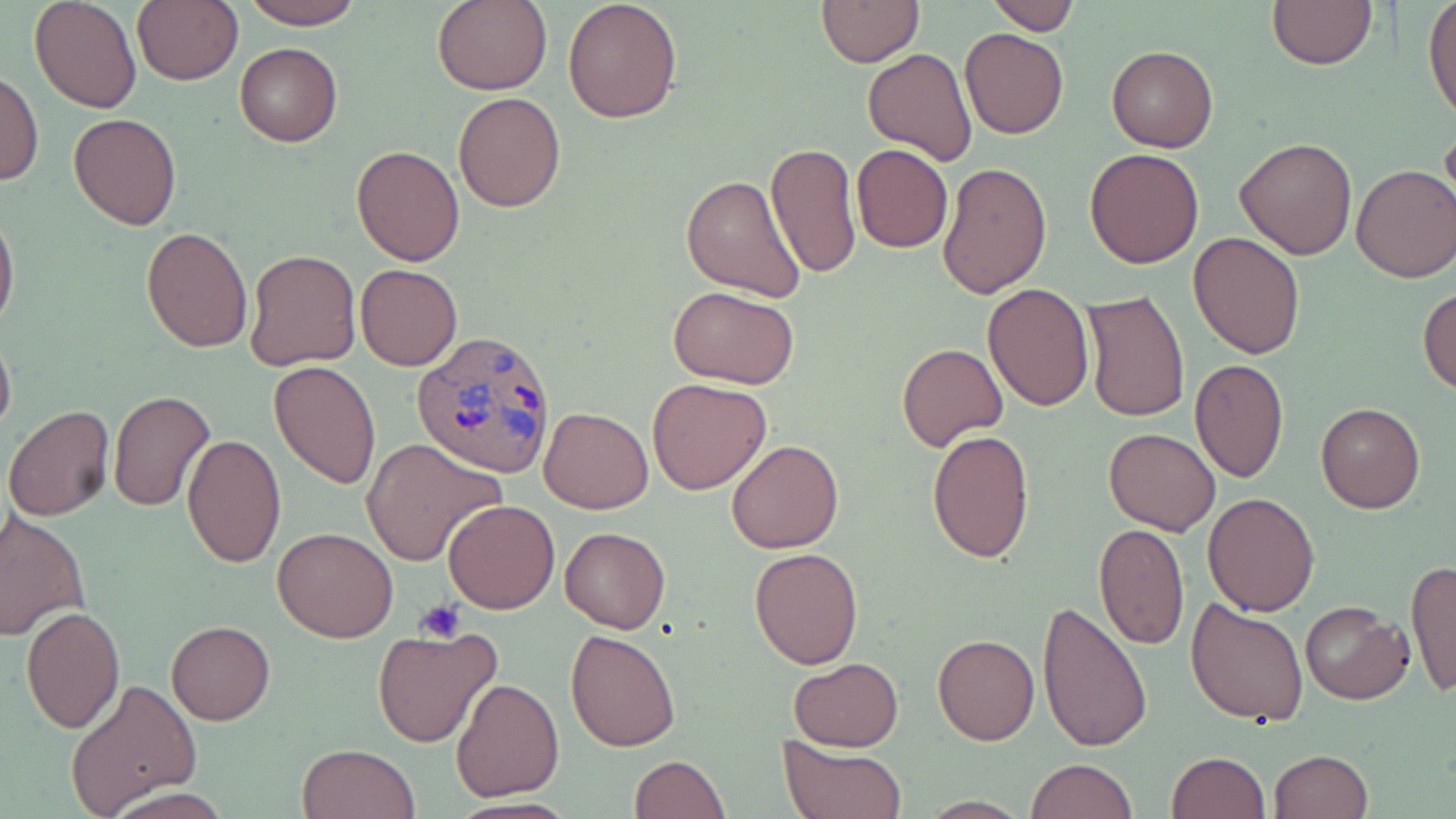 Approximate bounding boxes as [x1, y1, x2, y2] in pixels. Plasmodium ovale-infected red blood cell locations: [411, 327, 557, 476]. Uninfected red blood cell locations: [30, 0, 142, 112], [133, 0, 244, 86], [238, 0, 365, 30], [433, 0, 551, 94], [563, 0, 683, 123], [981, 0, 1080, 34], [1423, 0, 1455, 124], [815, 1, 923, 66], [1266, 2, 1379, 70], [960, 28, 1069, 140], [235, 42, 342, 146], [1106, 44, 1217, 151], [862, 46, 977, 166], [1, 69, 43, 189], [452, 92, 565, 213], [69, 112, 182, 231], [1440, 121, 1456, 221], [1235, 136, 1359, 258], [766, 143, 863, 279], [851, 143, 953, 253], [351, 145, 465, 265], [1084, 147, 1204, 269], [937, 162, 1052, 299], [1351, 164, 1456, 283], [681, 172, 808, 301], [0, 205, 19, 334], [140, 226, 253, 353], [1188, 231, 1306, 359], [244, 247, 362, 371], [355, 263, 461, 371], [982, 283, 1095, 411], [668, 285, 800, 389], [1418, 287, 1456, 398], [1080, 290, 1190, 425], [0, 329, 16, 442], [897, 343, 1007, 450], [1191, 356, 1289, 485], [269, 360, 382, 488], [648, 377, 772, 495], [108, 389, 218, 512], [1315, 402, 1425, 514], [4, 406, 117, 521], [538, 406, 654, 513], [926, 427, 1035, 564], [1103, 427, 1221, 535], [181, 432, 287, 569], [360, 439, 507, 566], [727, 439, 844, 554], [1203, 492, 1320, 615], [444, 499, 560, 615], [0, 510, 90, 641], [1094, 523, 1189, 650], [559, 526, 670, 633], [273, 527, 399, 643], [750, 547, 863, 668], [1405, 559, 1456, 698], [1186, 596, 1309, 725], [1037, 598, 1155, 752], [1301, 602, 1414, 704], [22, 605, 125, 733], [166, 620, 275, 724], [372, 626, 502, 748], [567, 628, 682, 752], [933, 633, 1040, 745], [788, 657, 905, 751], [449, 679, 564, 802], [64, 680, 203, 818], [777, 737, 908, 819], [297, 743, 421, 819], [1269, 748, 1373, 818], [1164, 751, 1270, 819], [628, 754, 730, 818], [1026, 758, 1137, 819], [102, 786, 235, 818]. Platelet locations: [415, 599, 466, 644]. Slide-level diagnosis: Plasmodium ovale. Single field of view. May-Grünwald-Giemsa stain. Thin blood film. Image is 1456×819 pixels. Optical microscopy. Captured at 1000x magnification.